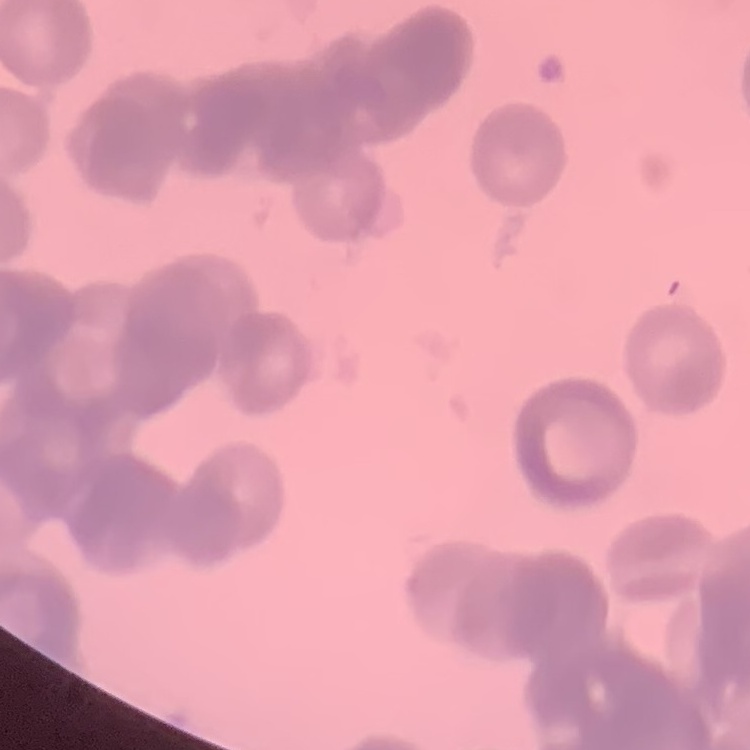

erythrocyte_morphology: rouleaux formation
stain: Field's or Giemsa
image_type: square crop of a larger photomicrograph
preparation: thin peripheral smear